Name the parasite shown.
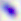
Toxoplasma gondii.

modality: photomicrograph
magnification: 400x